Name the parasite shown.
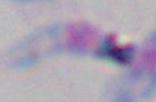
Toxoplasma gondii.

magnification = 1000x
modality = photomicrograph